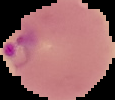

Summary:
  - Preparation: thin blood film
  - Image type: segmented cell region with the area outside set to black
  - Image size: 115×100 pixels
  - Result: Plasmodium parasites identified